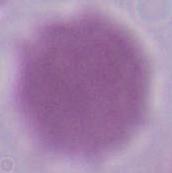

Summary:
  - Modality: micrograph
  - Identification: red blood cell
  - Magnification: 1000x